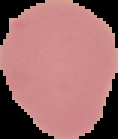 Segmented cell region on a black background. Image is 118×139 pixels. Malaria status: uninfected. From a thin blood film.